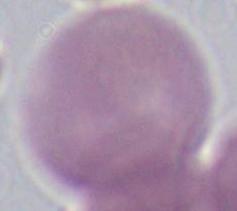

magnification: 1000x
modality: micrograph
identification: erythrocyte